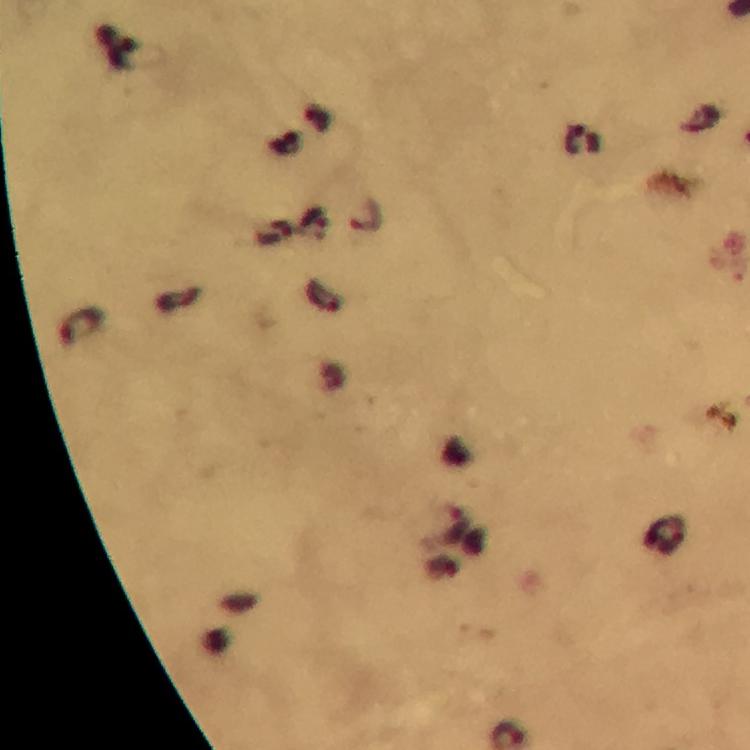

Approximate centers as [x, y] in pixels.
Summary:
  - Malaria parasite locations: [584, 142], [366, 216], [457, 524]
  - Immersion oil: applied
  - Image size: 750×750 pixels
  - Magnification: 100x
  - Preparation: thick blood smear
  - Cropped from: one field of view
  - Context: from a diagnostic examination for malaria
  - Capture: smartphone photograph through a microscope
  - Stain: Giemsa